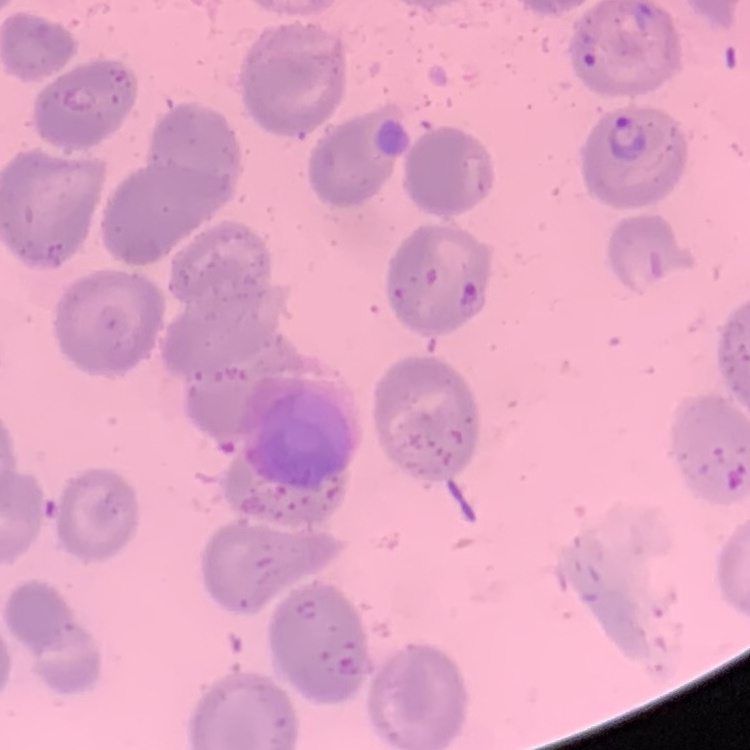

red_blood_cell_morphology: no rouleaux formation
image_type: one tile cut from a larger photomicrograph
stain: Field's or Giemsa
preparation: thin peripheral smear